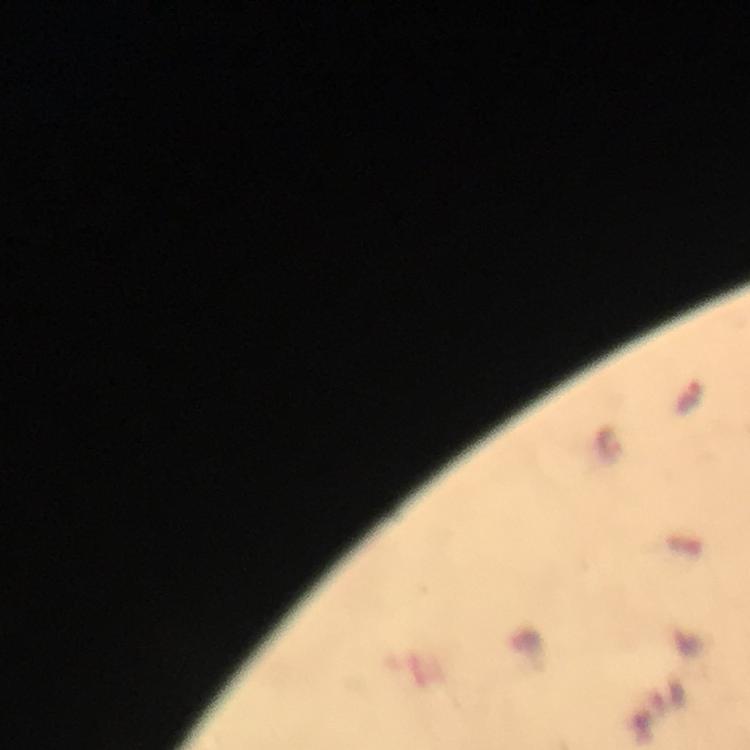

Approximate centers as (x, y) in pixels. Malaria parasite locations: (687, 397). Immersion oil applied. Image is 750×750 pixels. Thick blood film. Giemsa-stained preparation. Photographed with a smartphone mounted on the microscope. At 100x magnification. From a diagnostic examination for malaria. Cropped region of a single field of view.